Assess this cell for malaria.
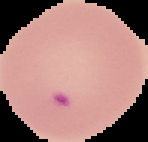

It is parasitized.

Summary:
  - Image type: segmented cell region with the area outside set to black
  - Preparation: thin blood film
  - Image size: 148×142 pixels